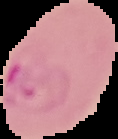

image type = segmented cell region on a black background
result = Plasmodium parasites identified
image size = 118×139 pixels
preparation = thin blood smear